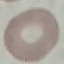
malaria status = uninfected
image type = cell patch, automatically extracted from a larger field of view and resized to 64 × 64 pixels
stain = Giemsa
preparation = thin blood smear
capture = smartphone camera at the microscope eyepiece